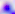

modality = micrograph
magnification = 400x
identification = Toxoplasma gondii